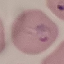

Malaria status: parasitized. Acquired by smartphone through the microscope eyepiece. Cell patch, automatically extracted from a larger field of view and resized to 64 × 64 pixels. Giemsa-stained preparation. Thin blood smear.